Describe the morphology of the red blood cells.
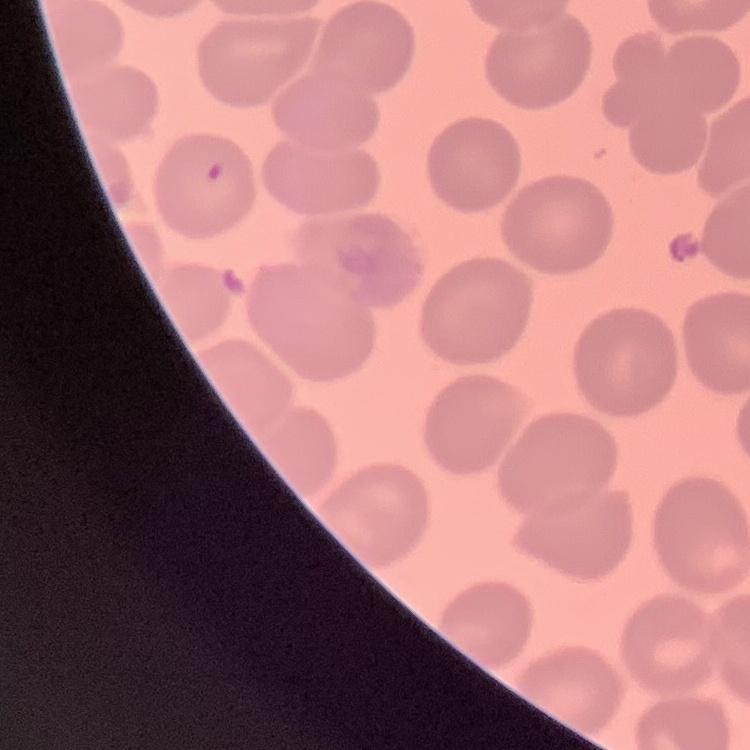

No rouleaux formation.

{
  "image_type": "square crop of a larger photomicrograph",
  "stain": "Field's or Giemsa",
  "preparation": "thin blood film"
}